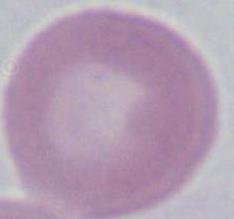
magnification = 1000x
modality = photomicrograph
identification = red blood cell